Assess this cell for malaria.
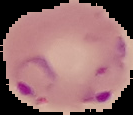

Parasitized.

Summary:
  - Image type: segmented cell region on a black background
  - Image size: 133×115 pixels
  - Preparation: thin blood film